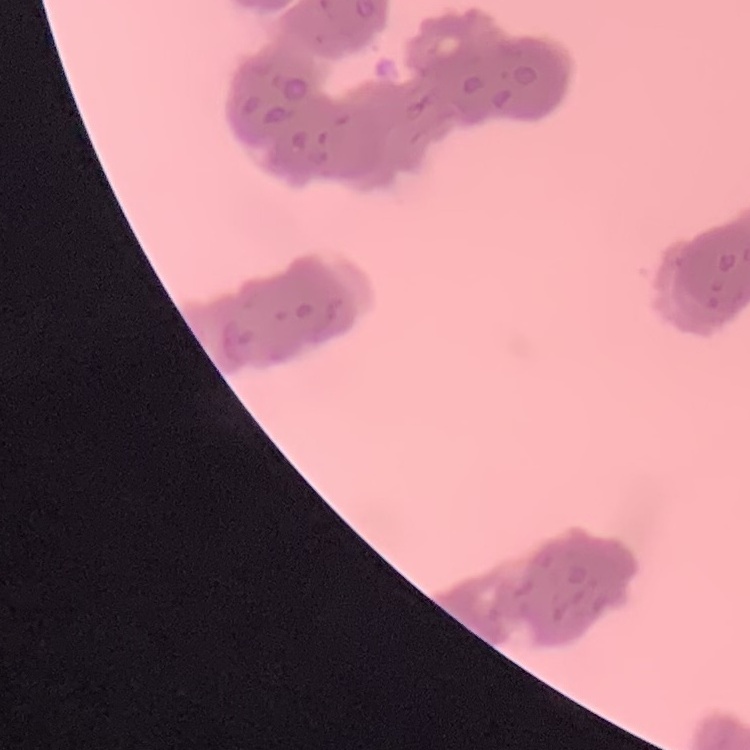

red blood cell morphology = rouleaux formation
preparation = thin blood smear
stain = Field's or Giemsa
image type = square crop of a larger photomicrograph